Identify the parasite.
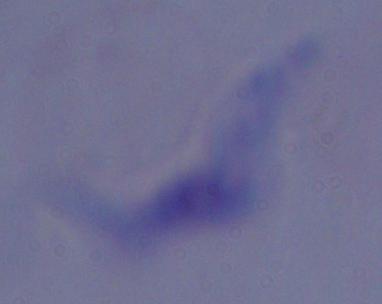
A trypanosome.

{
  "magnification": "1000x",
  "modality": "photomicrograph"
}